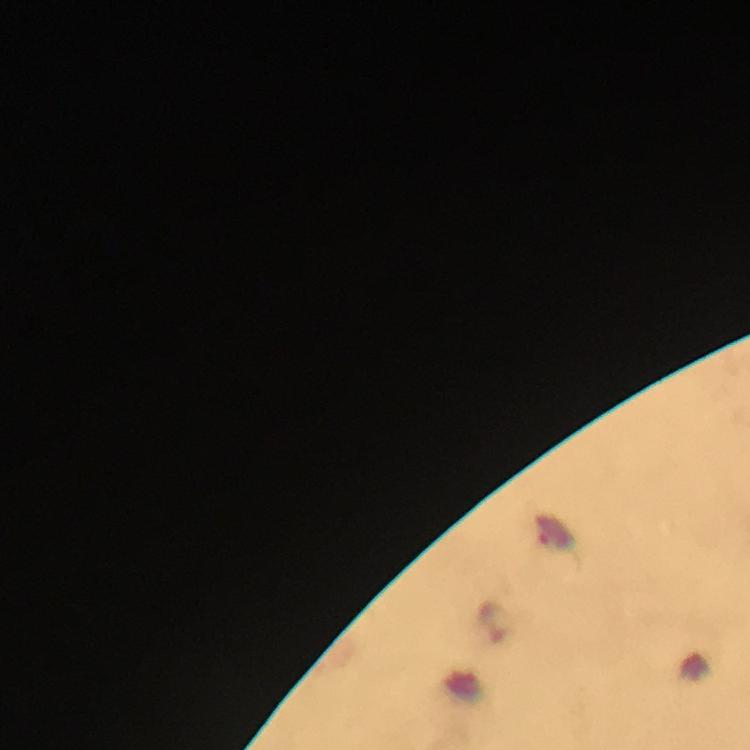 Approximate centers as (x, y) in pixels. Malaria parasite locations: (555, 535), (495, 622). Giemsa stain. Cropped region of a single field of view. At 100x magnification. Photographed through the microscope with a smartphone camera. Immersion oil applied. From a malaria diagnostic workup. Image is 750×750 pixels. Thick smear.